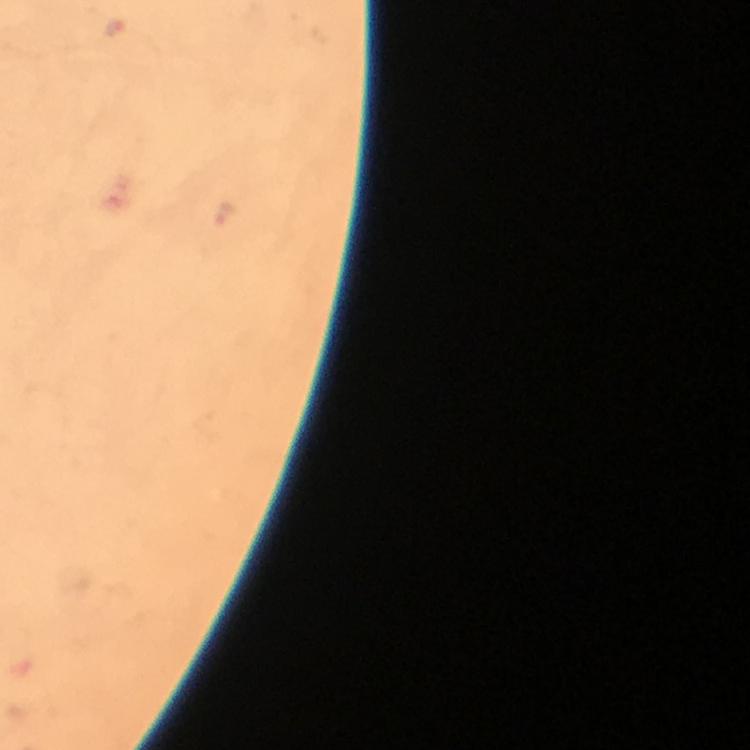

immersion oil = used
Plasmodium parasite locations = approximate centers as {x, y} in pixels: {114, 27}
stain = Giemsa
magnification = 100x
preparation = thick blood smear
capture = smartphone camera through the microscope
image size = 750×750 pixels
context = from a diagnostic examination for malaria
cropped from = a single field of view